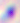 Toxoplasma gondii is seen. Micrograph. 400x magnification.